State the blood parasite species.
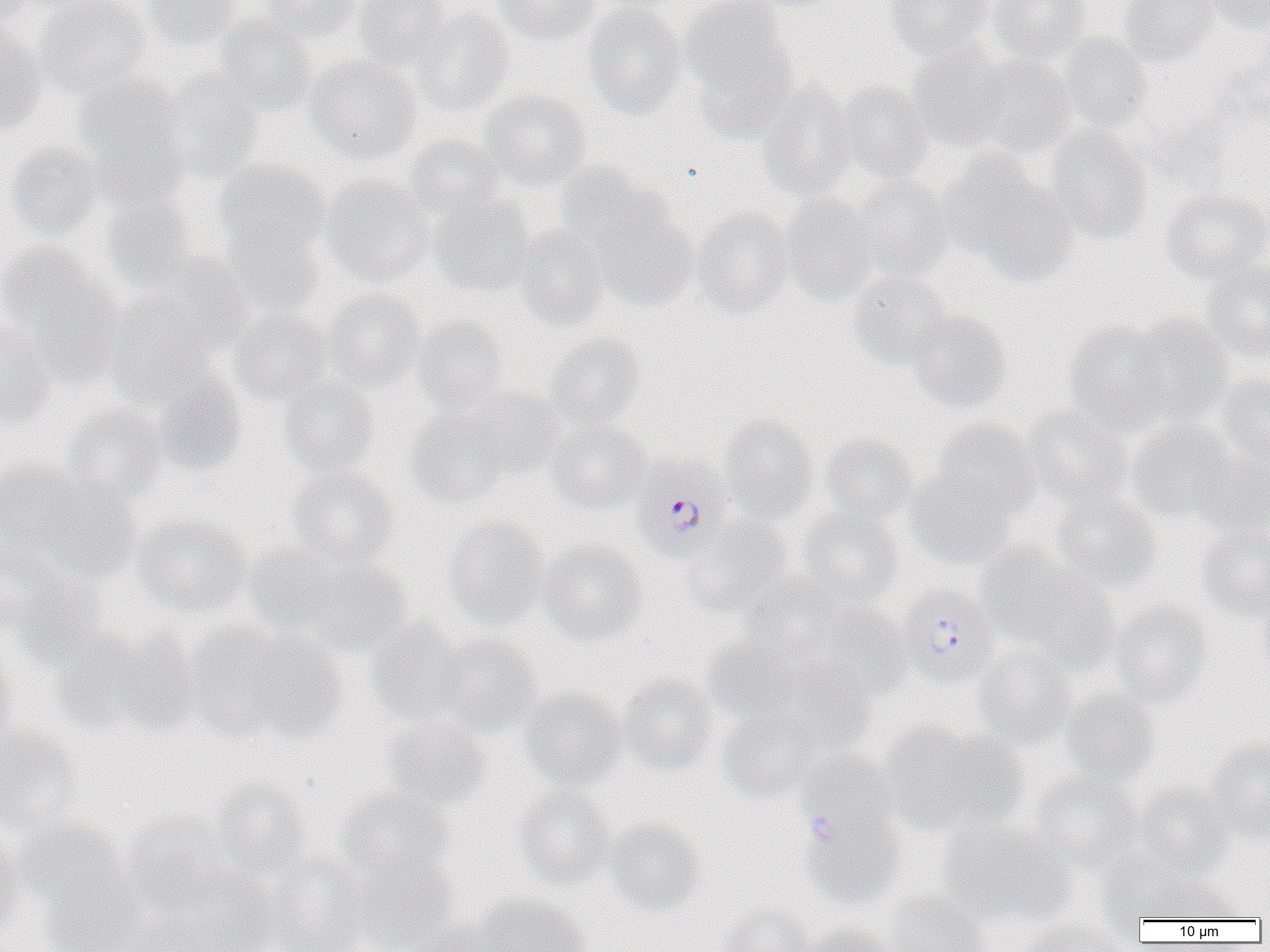
Plasmodium falciparum.

Approximate bounding boxes as (x1,y1)-(x2,y2) corner pairs in pixels. Plasmodium falciparum-infected red blood cell locations: (631,456)-(733,562), (898,586)-(999,689). Uninfected red blood cell locations: (0,0)-(39,25), (34,0)-(152,100), (140,0)-(243,50), (261,0)-(362,43), (354,0)-(451,72), (492,0)-(600,46), (680,0)-(798,107), (743,0)-(845,13), (884,0)-(994,60), (987,0)-(1091,64), (1119,0)-(1219,67), (1205,0)-(1270,36), (584,3)-(689,122), (411,8)-(514,118), (213,15)-(317,116), (0,26)-(47,137), (1059,34)-(1152,133), (907,42)-(1014,152), (968,53)-(1079,159), (304,57)-(423,164), (161,69)-(263,182), (74,75)-(187,191), (753,80)-(857,202), (836,81)-(934,184), (479,90)-(592,191), (1044,128)-(1153,244), (403,135)-(505,221), (5,143)-(105,243), (941,152)-(1075,284), (215,160)-(330,259), (554,161)-(667,254), (846,174)-(955,282), (320,175)-(434,286), (1161,189)-(1270,286), (428,192)-(535,298), (780,195)-(880,305), (100,197)-(200,296), (691,208)-(794,318), (591,209)-(698,312), (220,224)-(324,318), (512,227)-(610,332), (1,242)-(110,357), (147,255)-(255,350), (1200,262)-(1270,365), (847,272)-(953,371), (321,289)-(426,391), (105,296)-(218,405), (227,308)-(332,405), (905,308)-(1012,414), (1125,315)-(1235,427), (411,316)-(508,416), (0,318)-(57,430), (1063,320)-(1175,435), (545,333)-(646,431), (1214,370)-(1270,476), (154,371)-(247,476), (278,377)-(378,478), (460,387)-(563,479), (58,405)-(167,510), (1023,405)-(1134,512), (406,407)-(511,509), (718,415)-(821,525), (544,420)-(650,515), (930,420)-(1039,519), (1126,420)-(1240,525), (818,434)-(920,527), (1188,455)-(1270,542), (0,457)-(86,559), (286,467)-(398,568), (906,471)-(1017,570), (34,483)-(141,584), (1050,491)-(1161,595), (797,508)-(904,607), (132,514)-(251,619), (686,516)-(793,616), (442,517)-(550,631), (1196,526)-(1270,623), (538,539)-(645,645), (241,543)-(348,639), (976,544)-(1083,648), (0,546)-(105,665), (299,557)-(413,658), (1016,569)-(1120,674), (742,575)-(847,662), (1256,592)-(1270,690), (1109,599)-(1215,708), (811,601)-(913,703), (366,620)-(471,728), (182,621)-(296,742), (54,623)-(194,738), (236,629)-(349,743), (433,632)-(543,737), (702,639)-(801,725), (0,643)-(17,755), (973,645)-(1077,747), (619,674)-(720,776), (518,687)-(627,792), (1059,691)-(1161,790), (717,708)-(824,803), (378,715)-(491,813), (881,721)-(1023,837), (0,729)-(83,834), (1205,738)-(1270,844), (796,751)-(897,839), (1029,773)-(1144,875), (208,781)-(314,884), (1133,784)-(1233,880), (513,786)-(616,890), (336,789)-(454,884), (120,809)-(237,914), (803,812)-(905,911), (13,817)-(131,918), (603,818)-(706,916), (939,821)-(1072,929), (0,828)-(26,938), (348,852)-(459,951), (266,855)-(373,952), (178,871)-(283,952), (1134,872)-(1241,922), (36,873)-(146,952), (883,890)-(990,952), (472,894)-(590,952), (716,904)-(813,952), (116,910)-(217,952), (405,918)-(508,952), (1021,919)-(1132,952), (805,923)-(899,952). Image is 1270×952 pixels. Captured at 1000x magnification. Thin blood film. One field of a larger specimen. Optical microscopy.